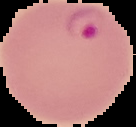
{
  "result": "malaria parasites detected",
  "preparation": "thin blood film",
  "image_type": "cell region segmented out of the field of view; surrounding area masked to black",
  "image_size": "136×127 pixels"
}